Report the malaria status of this cell.
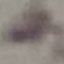

It is uninfected.

{
  "capture": "smartphone camera at the microscope eyepiece",
  "image_type": "automatically extracted cell patch, resized to 64 × 64 pixels",
  "stain": "Giemsa",
  "preparation": "thin smear"
}